Name the parasite shown.
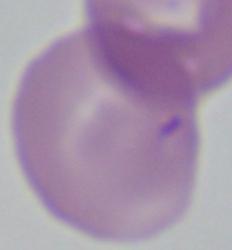
This is Babesia.

Summary:
  - Modality: photomicrograph
  - Magnification: 1000x